Comment on the morphology of the red blood cells.
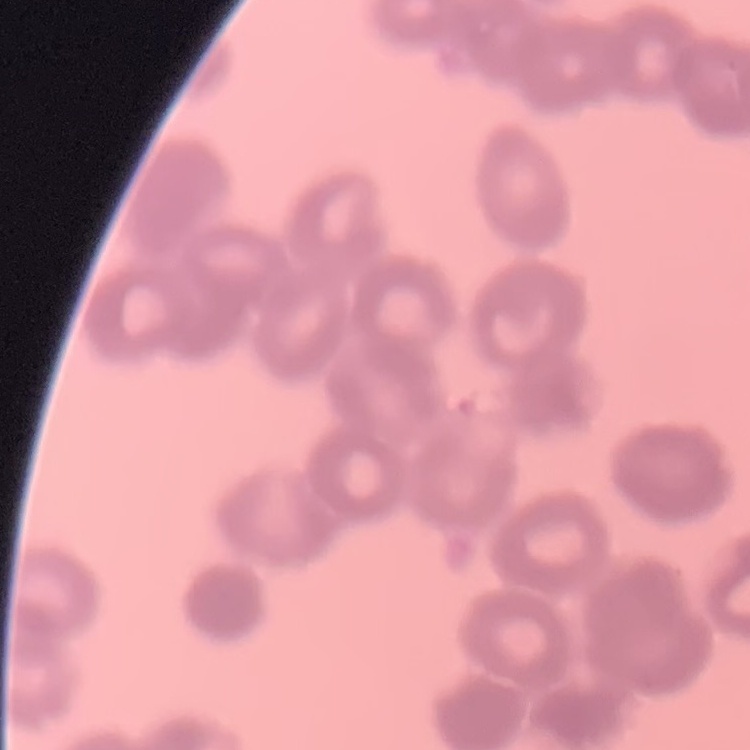

They show rouleaux formation.

Summary:
  - Preparation: thin blood film
  - Image type: one tile cut from a larger photomicrograph
  - Stain: Field's or Giemsa